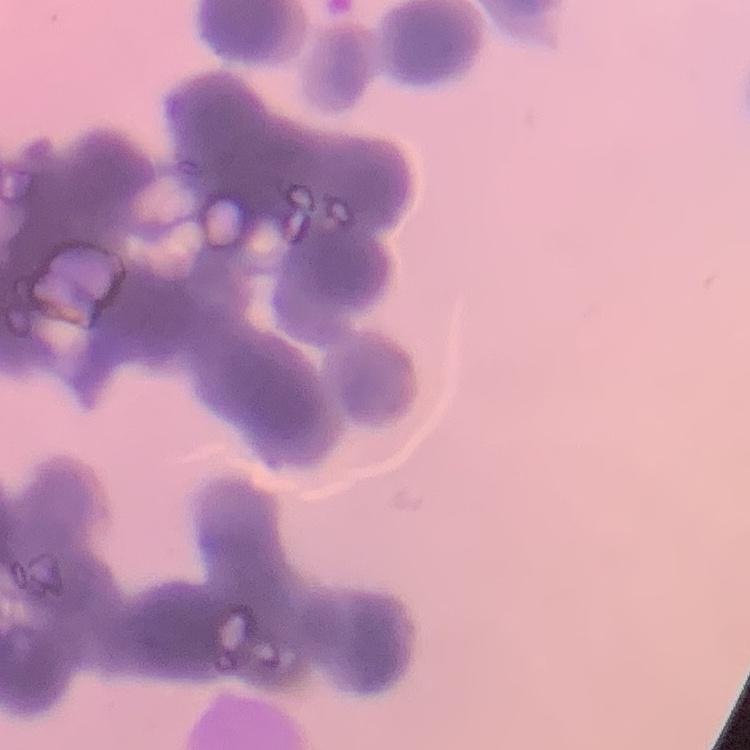

Summary:
  - Erythrocyte morphology: rouleaux formation
  - Preparation: thin peripheral smear
  - Image type: square crop of a larger photomicrograph
  - Stain: Field's or Giemsa